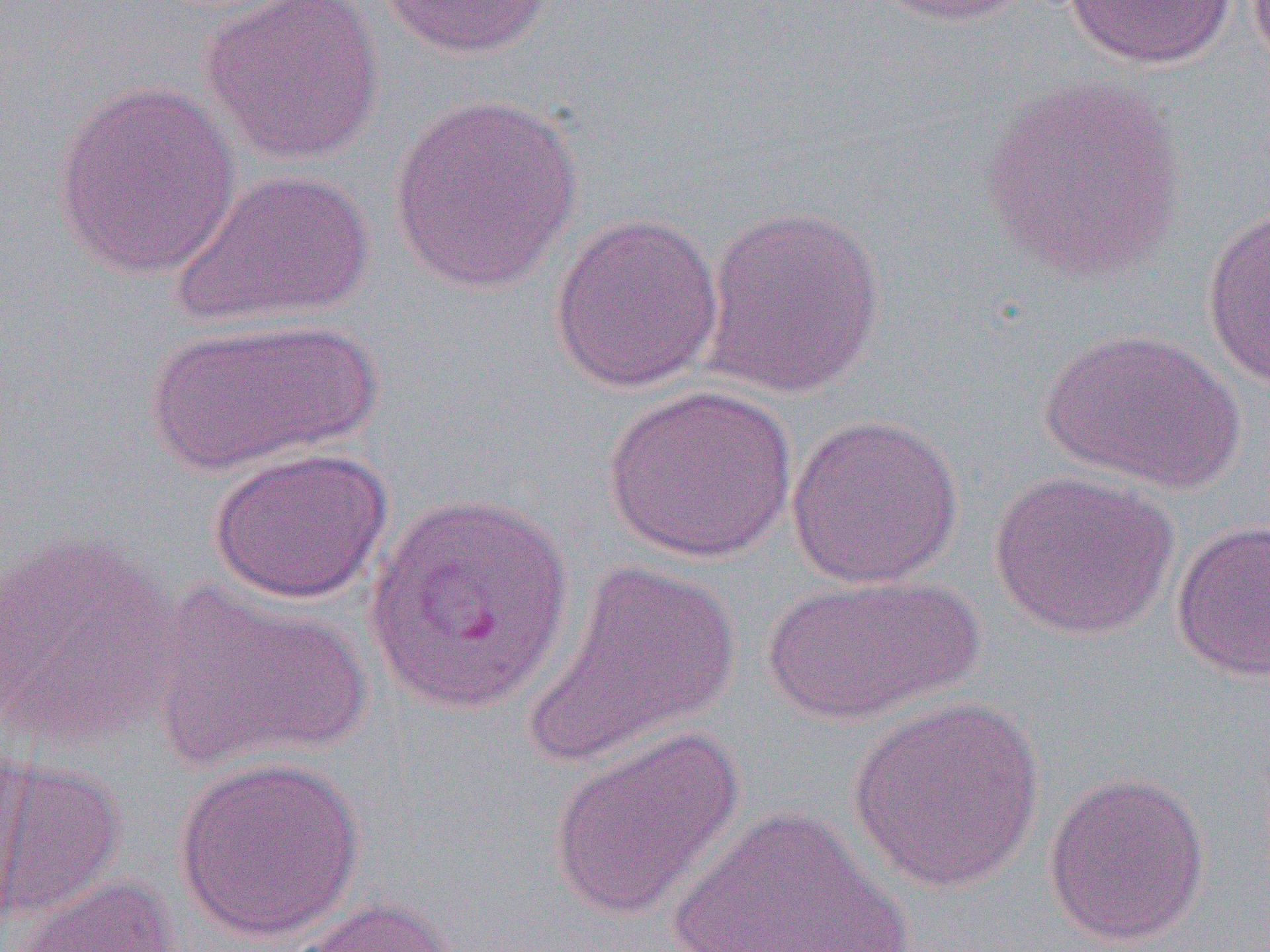 Approximate bounding boxes as named x1/y1/x2/y2 corners in pixels. Plasmodium vivax-infected red blood cell locations: (x1=364, y1=489, x2=574, y2=715). Uninfected red blood cell locations: (x1=198, y1=0, x2=386, y2=168), (x1=379, y1=0, x2=555, y2=59), (x1=864, y1=0, x2=1033, y2=27), (x1=1063, y1=0, x2=1236, y2=69), (x1=979, y1=74, x2=1189, y2=282), (x1=50, y1=81, x2=241, y2=281), (x1=388, y1=93, x2=584, y2=294), (x1=169, y1=168, x2=376, y2=330), (x1=700, y1=204, x2=886, y2=399), (x1=1200, y1=204, x2=1270, y2=393), (x1=549, y1=212, x2=725, y2=394), (x1=144, y1=316, x2=380, y2=476), (x1=1039, y1=328, x2=1245, y2=495), (x1=602, y1=384, x2=798, y2=565), (x1=785, y1=413, x2=965, y2=589), (x1=206, y1=446, x2=394, y2=604), (x1=988, y1=469, x2=1180, y2=641), (x1=1170, y1=518, x2=1270, y2=683), (x1=0, y1=529, x2=180, y2=753), (x1=526, y1=560, x2=742, y2=769), (x1=761, y1=574, x2=982, y2=726), (x1=148, y1=583, x2=370, y2=770), (x1=846, y1=695, x2=1045, y2=895), (x1=546, y1=725, x2=746, y2=922), (x1=173, y1=756, x2=366, y2=944), (x1=0, y1=758, x2=125, y2=927), (x1=1043, y1=771, x2=1211, y2=948), (x1=662, y1=806, x2=914, y2=951), (x1=13, y1=874, x2=180, y2=952), (x1=282, y1=896, x2=458, y2=952). Slide-level diagnosis: Plasmodium vivax. Thin blood film. Single field of view. Captured at 1000x magnification. Light microscopy. Image is 1270×952 pixels.